Comment on the morphology of the erythrocytes.
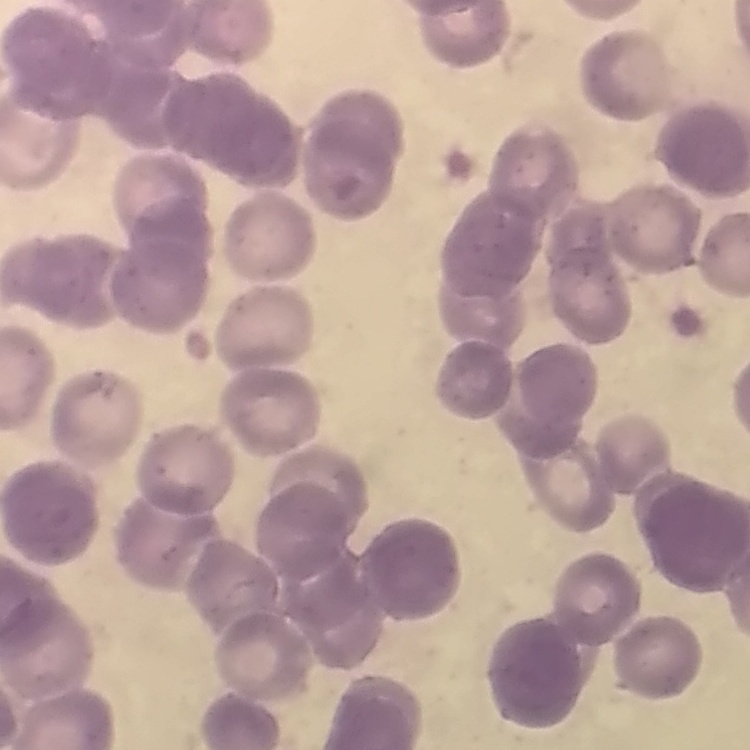
They show rouleaux formation.

preparation = thin blood smear
image type = one tile cut from a larger photomicrograph
stain = Field's or Giemsa